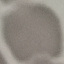 Malaria status: uninfected. Giemsa-stained preparation. Thin smear of blood. Acquired by smartphone through the microscope eyepiece. Cell patch, automatically extracted from a larger field of view and resized to 64 × 64 pixels.